Find each parasitized RBC.
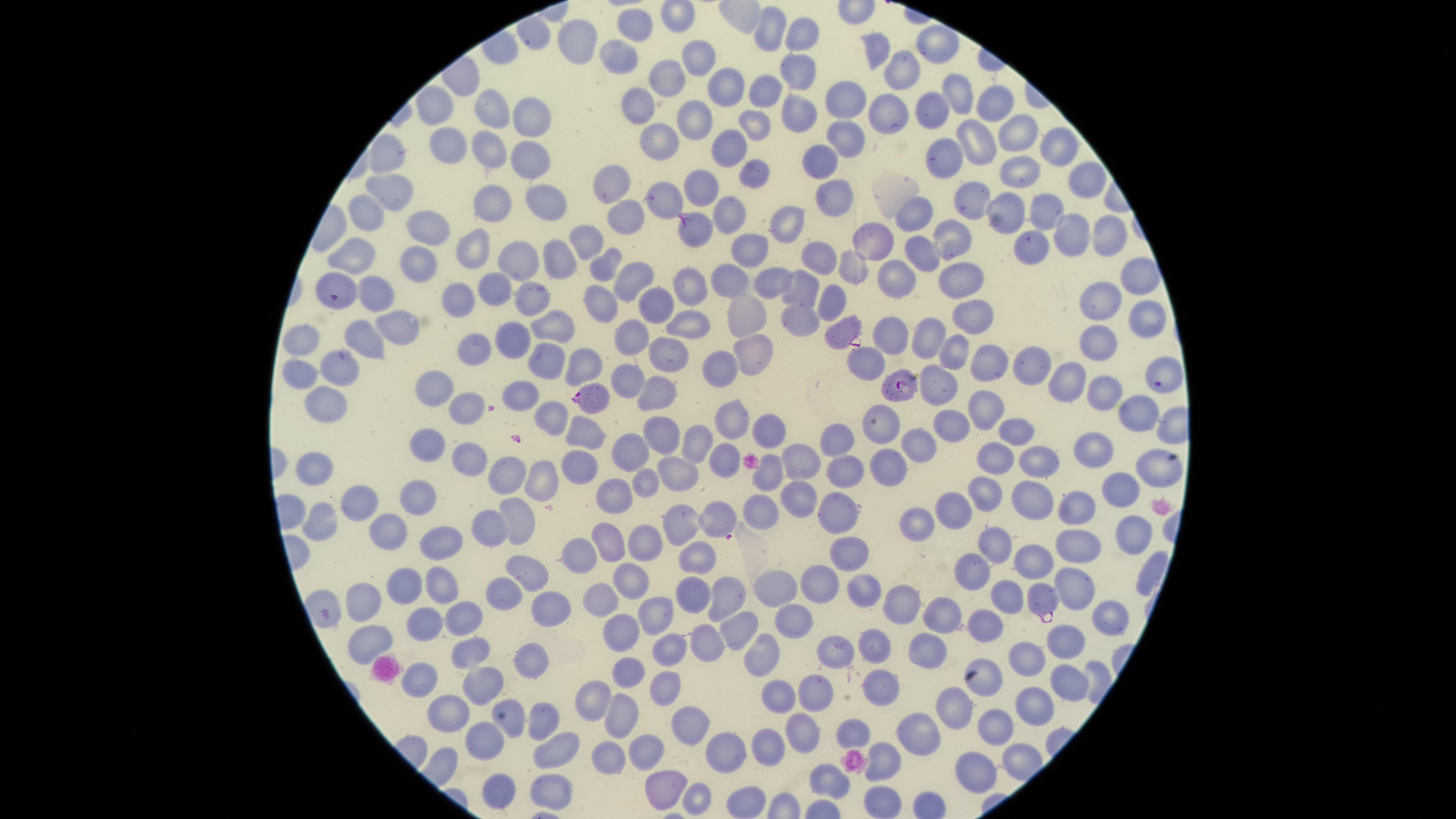
Approximate marker points as [x, y] in pixels.
Parasitized RBCs: [694, 230], [841, 333], [899, 384], [1160, 385], [592, 398], [1042, 600].

{
  "species": "Plasmodium falciparum",
  "field_of_view": "single",
  "stain": "Giemsa",
  "image_size": "1456×819 pixels",
  "preparation": "thin blood smear",
  "uninfected_RBCs": "approximate marker points as [x, y] in pixels: [773, 29], [640, 32], [806, 36], [577, 41], [938, 45], [875, 46], [700, 55], [622, 63], [798, 68], [901, 68], [662, 78], [719, 82], [766, 92], [953, 92], [848, 99], [995, 99], [641, 103], [436, 106], [494, 109], [803, 110], [531, 112], [935, 113], [894, 115], [695, 116], [753, 127], [852, 130], [1015, 130], [664, 138], [447, 142], [734, 145], [980, 145], [1055, 145], [487, 148], [523, 155], [812, 156], [947, 156], [390, 162], [1013, 170], [755, 173], [1082, 175], [705, 182], [606, 185], [390, 191], [666, 195], [495, 196], [545, 198], [827, 198], [974, 198], [373, 205], [728, 212], [1005, 212], [1044, 214], [910, 217], [622, 219], [425, 226], [1114, 226], [781, 227], [1072, 234], [946, 237], [1030, 240], [587, 241], [880, 241], [468, 245], [920, 247], [752, 248], [812, 252], [552, 254], [509, 255], [362, 257], [418, 262], [602, 262], [859, 262], [1131, 266], [959, 272], [894, 273], [627, 277], [338, 280], [727, 280], [775, 280], [493, 283], [797, 289], [375, 290], [530, 291], [460, 292], [690, 294], [594, 298], [1097, 298], [649, 303], [836, 306], [746, 311], [796, 317], [1148, 319], [689, 320], [391, 321], [966, 326], [558, 327], [629, 335], [363, 337], [930, 337], [1105, 338], [309, 339], [510, 341], [895, 341], [752, 348], [958, 348], [480, 352], [663, 352], [583, 357], [537, 359], [716, 362], [864, 362], [991, 364], [304, 370], [347, 370], [1036, 370], [630, 376], [1065, 379], [945, 386], [437, 387], [524, 391], [1100, 392], [656, 395], [325, 398], [466, 407], [985, 409], [1137, 411], [550, 415], [885, 419], [731, 420], [952, 423], [1012, 430], [585, 433], [663, 434], [767, 435], [926, 437], [427, 440], [698, 440], [834, 440], [641, 444], [1094, 448], [726, 452], [470, 454], [998, 455], [580, 461], [1042, 461], [1151, 462], [806, 464], [677, 465], [888, 465], [844, 466], [314, 469], [509, 471], [648, 475], [772, 477], [542, 479], [1118, 487], [982, 489], [621, 491], [798, 494], [1030, 494], [422, 496], [1080, 499], [361, 500], [952, 505], [762, 507], [834, 510], [516, 514], [717, 517], [677, 518], [919, 520], [328, 523], [488, 524], [390, 531], [1130, 531], [441, 538], [611, 539], [648, 541], [997, 542], [1082, 546], [698, 549], [849, 552], [586, 555], [1030, 560], [972, 564], [527, 569], [630, 577], [818, 581], [1074, 582], [441, 584], [776, 585], [867, 585], [1005, 587], [408, 588], [509, 589], [605, 595], [692, 595], [727, 595], [902, 604], [374, 609], [548, 610], [420, 612], [664, 613], [791, 614], [462, 616], [941, 616], [1109, 616], [739, 627], [986, 627], [628, 630], [374, 639], [708, 641], [1064, 644], [877, 647], [837, 648], [669, 649], [766, 649], [470, 651], [928, 651], [1027, 659], [527, 661], [634, 669], [420, 676], [987, 679], [480, 680], [1071, 680], [664, 684], [887, 687], [813, 691], [777, 694], [599, 698], [954, 700], [1034, 705], [453, 714], [620, 716], [516, 721], [543, 721], [685, 721], [999, 725], [803, 730], [852, 730], [920, 738], [487, 740], [774, 740], [562, 747], [608, 748], [646, 748], [729, 754], [887, 757], [982, 770], [826, 776], [666, 780], [552, 788], [698, 793], [507, 798]",
  "visible_region": "circular",
  "capture": "smartphone photograph through the microscope eyepiece"
}